Classify this cell by malaria status.
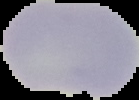

Uninfected.

Summary:
  - Preparation: thin blood smear
  - Image type: segmented cell region with the area outside set to black
  - Image size: 139×100 pixels